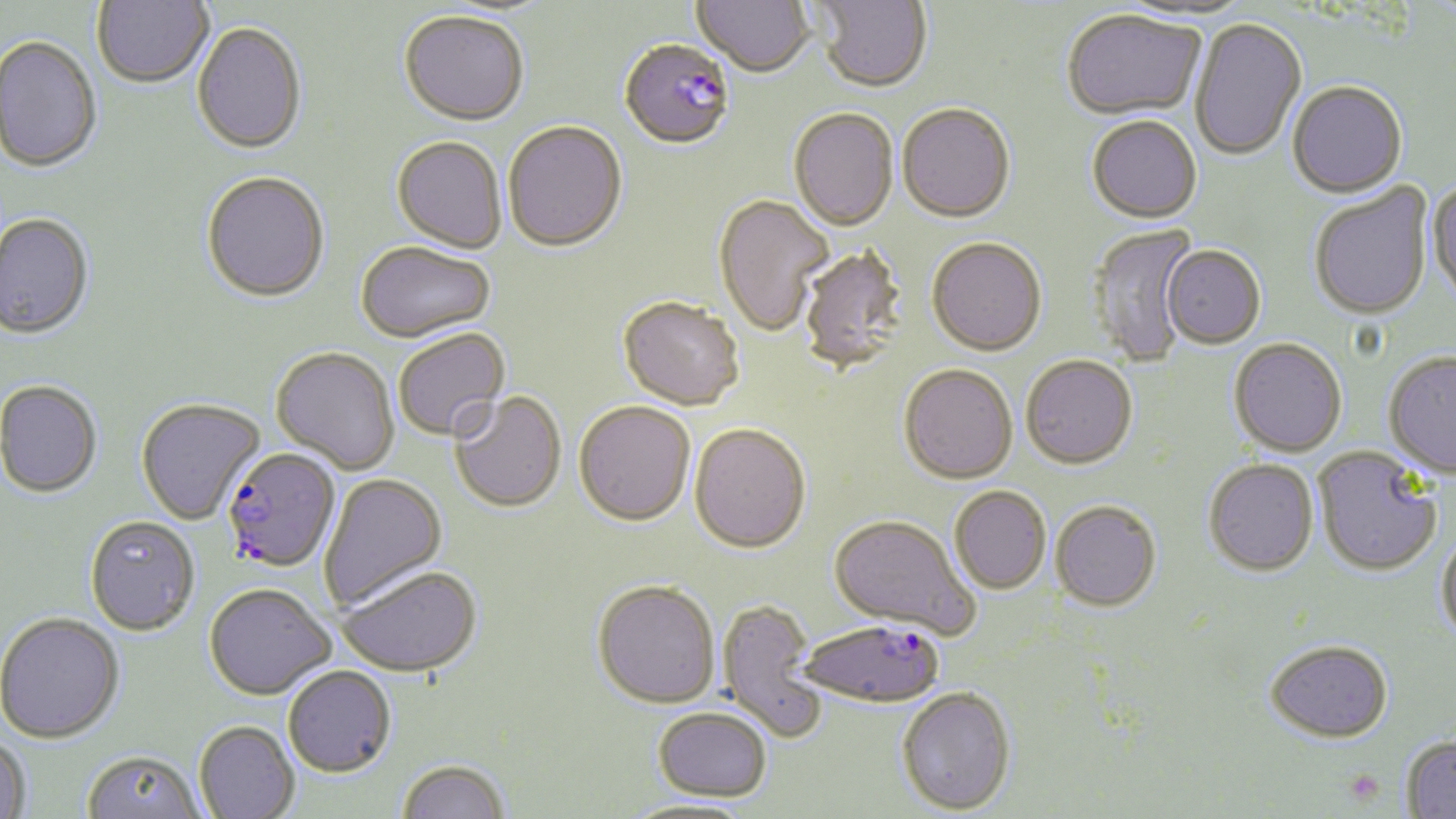
Approximate bounding boxes as (x1, y1, x2, y2) in pixels. Uninfected red blood cell locations: (91, 0, 214, 88), (693, 0, 814, 78), (812, 0, 933, 94), (399, 11, 530, 127), (1062, 12, 1206, 123), (1190, 19, 1307, 162), (192, 22, 308, 154), (0, 34, 102, 173), (1287, 82, 1408, 200), (897, 105, 1016, 226), (788, 108, 898, 232), (1087, 118, 1202, 225), (503, 122, 627, 253), (391, 137, 508, 254), (201, 171, 330, 301), (1426, 180, 1456, 308), (1308, 185, 1433, 323), (713, 194, 833, 337), (0, 212, 95, 338), (1085, 223, 1200, 368), (926, 238, 1047, 358), (355, 242, 496, 343), (797, 246, 909, 373), (1162, 246, 1265, 350), (618, 296, 744, 410), (392, 328, 511, 442), (1228, 338, 1347, 458), (271, 346, 400, 474), (1383, 352, 1456, 480), (1021, 356, 1138, 470), (898, 363, 1018, 484), (0, 379, 103, 497), (449, 390, 567, 512), (136, 397, 265, 524), (574, 401, 696, 526), (690, 422, 811, 552), (1313, 447, 1442, 578), (1203, 459, 1319, 577), (318, 472, 447, 611), (949, 486, 1051, 594), (1049, 499, 1161, 612), (828, 513, 979, 638), (84, 515, 200, 635), (1436, 530, 1456, 645), (337, 565, 482, 678), (592, 579, 720, 708), (204, 583, 335, 700), (717, 600, 828, 743), (0, 611, 124, 743), (1265, 641, 1393, 743), (282, 665, 396, 777), (896, 687, 1016, 814), (652, 706, 772, 801), (194, 721, 299, 819), (0, 735, 32, 817), (1401, 735, 1456, 818), (82, 749, 206, 819), (395, 758, 512, 819), (620, 798, 759, 818). Plasmodium falciparum-infected red blood cell locations: (621, 42, 735, 148), (221, 447, 340, 572), (797, 618, 945, 707). Platelet locations: (1341, 769, 1386, 808). Slide-level diagnosis: Plasmodium falciparum. Light microscopy. Image is 1456×819 pixels. One field of a larger specimen. Thin blood smear. May-Grünwald-Giemsa stain. 1000x magnification.